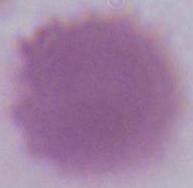

A red blood cell is seen. Captured at 1000x magnification. Micrograph.